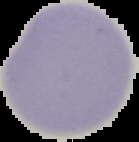 Image is 139×142 pixels. Segmented cell region on a black background. Result: negative for Plasmodium parasites. From a thin blood smear.